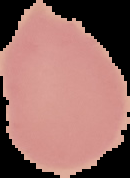

Summary:
  - Image size: 130×178 pixels
  - Preparation: thin blood smear
  - Malaria status: uninfected
  - Image type: segmented cell region on a black background